State which parasite is depicted.
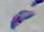

This is Toxoplasma gondii.

Summary:
  - Magnification: 1000x
  - Modality: micrograph